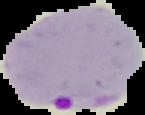 Malaria status: parasitized. From a thin blood smear. The area outside the segmented cell region is set to black. Image is 145×115 pixels.